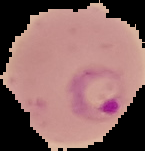

Malaria status: parasitized. Image is 145×151 pixels. From a thin blood film. The area outside the segmented cell region is set to black.